State the preparation type.
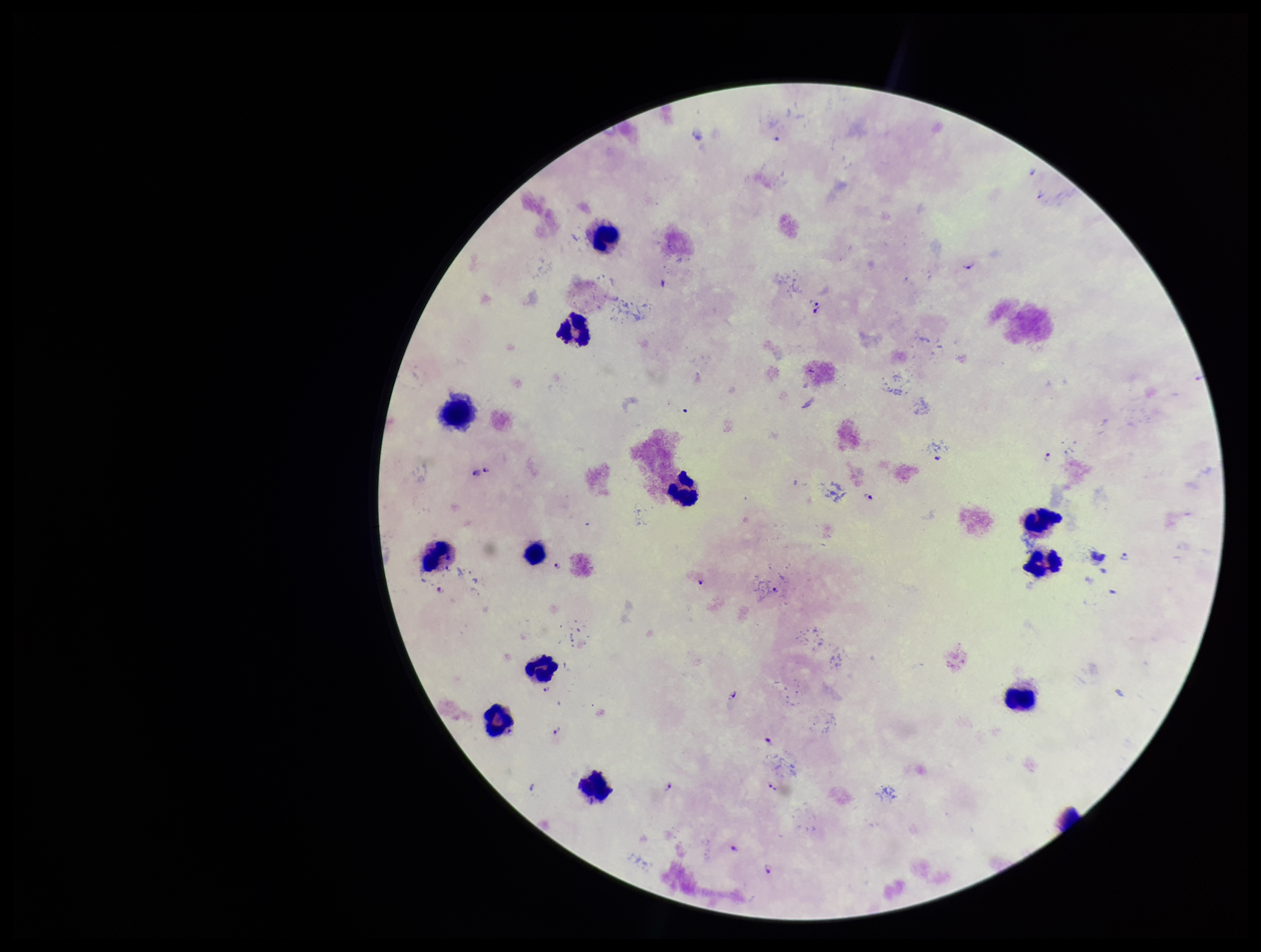

A thick smear.

Photographed through the microscope eyepiece with a smartphone camera. Plasmodium parasites: seen. Leukocyte count: 12. Stained with Giemsa. Parasite count: 14. One field from this slide. Species reported for this patient: Plasmodium falciparum. Patient malaria status: positive. Image is 1261×952 pixels.